Classify this cell by malaria status.
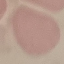

Uninfected.

Giemsa-stained preparation. Thin blood smear. Acquired by smartphone through the microscope eyepiece. Cell patch, automatically extracted from a larger field of view and resized to 64 × 64 pixels.